Report the malaria status of this cell.
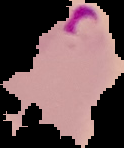
Parasitized.

The area outside the segmented cell region is set to black. From a thin blood film. Image is 124×148 pixels.